Comment on the morphology of the red blood cells.
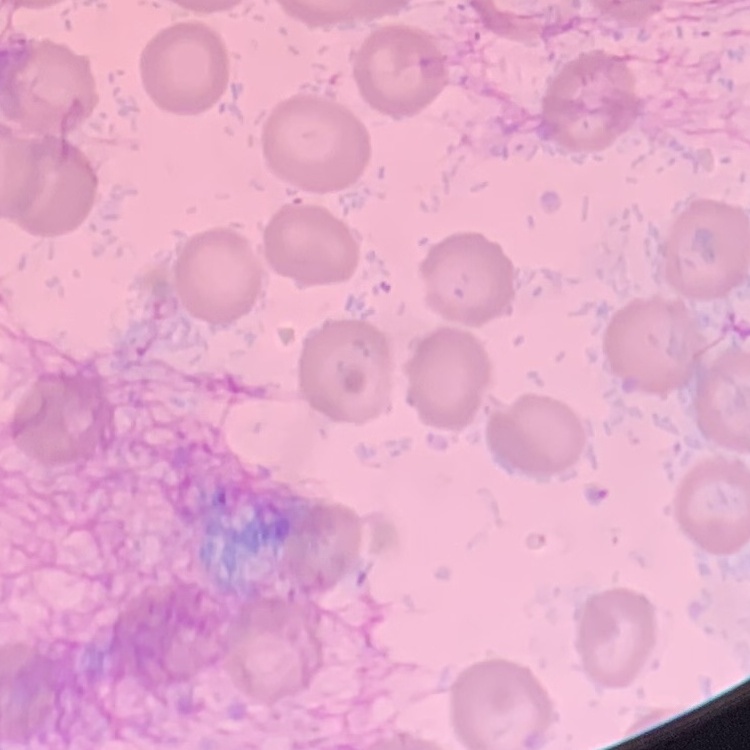
They show no rouleaux formation.

Thin blood film. Square crop of a larger photomicrograph. Stained with either Field's or Giemsa.